Assess the morphology of the erythrocytes.
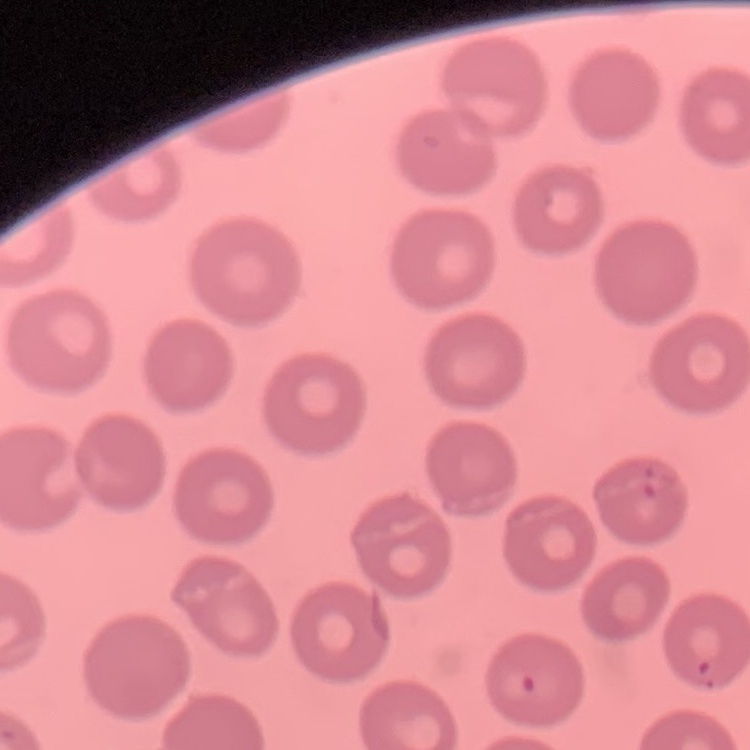
No rouleaux formation.

Thin blood smear. Field's or Giemsa stain. One tile cut from a larger photomicrograph.